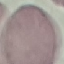
Summary:
  - Malaria status: uninfected
  - Stain: Giemsa
  - Capture: smartphone through the microscope eyepiece
  - Image type: automatically extracted cell patch, resized to 64 × 64 pixels
  - Preparation: thin blood smear